Locate every malaria parasite.
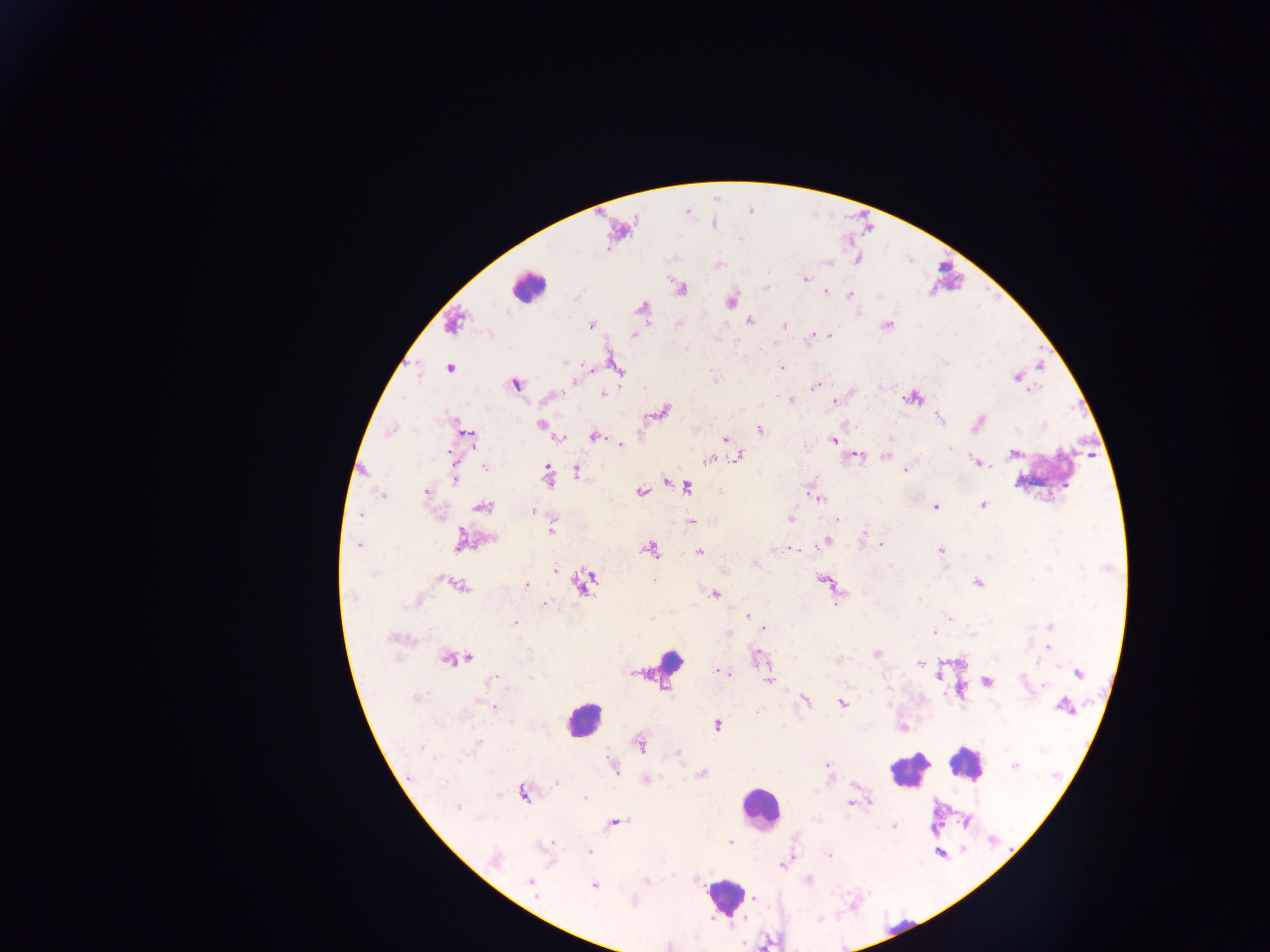
Approximate centers as (x, y) in pixels.
Malaria parasites: (807, 278), (824, 293), (851, 296), (859, 314), (679, 323), (592, 324), (783, 325), (830, 336), (808, 338), (687, 347), (566, 363), (593, 366), (449, 368), (782, 368), (572, 383), (815, 386), (1032, 393), (603, 394), (790, 400), (834, 401), (981, 420), (539, 425), (758, 429), (724, 439), (832, 439), (621, 445), (946, 446), (449, 450), (859, 456), (885, 456), (484, 468), (545, 468), (905, 470), (456, 480), (380, 493), (425, 493), (806, 494), (821, 498), (982, 504), (935, 506), (534, 512), (359, 513), (789, 519), (836, 519), (689, 522), (551, 528), (864, 533), (827, 540), (882, 544), (360, 545), (773, 549), (941, 550), (794, 551), (699, 552), (988, 559), (756, 562), (555, 570), (654, 583), (977, 583), (527, 585), (543, 604), (748, 615), (515, 623), (764, 628), (932, 631), (729, 633), (528, 650), (724, 673), (492, 682), (506, 686), (804, 700), (843, 703), (493, 707), (718, 725), (478, 742), (678, 753), (1014, 766), (829, 768), (614, 771), (701, 772), (647, 778), (558, 782), (582, 798), (869, 803), (848, 805), (456, 806), (892, 827), (729, 843), (591, 853), (829, 855), (782, 865), (530, 884), (594, 885), (537, 896).

Leukocyte locations: (528, 285), (581, 715). Thick blood film. Single field of view. Image is 1270×952 pixels. Mobile-phone photograph taken through the microscope. Collected in Ghana.